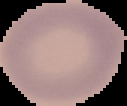
From a thin blood smear. Malaria status: uninfected. Segmented cell region on a black background. Image is 127×106 pixels.